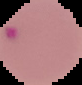
preparation = thin blood film
result = malaria parasites identified
image size = 82×85 pixels
image type = segmented cell region with the area outside set to black